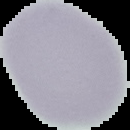

Summary:
  - Image type: segmented cell region with the area outside set to black
  - Malaria status: uninfected
  - Image size: 130×130 pixels
  - Preparation: thin blood smear